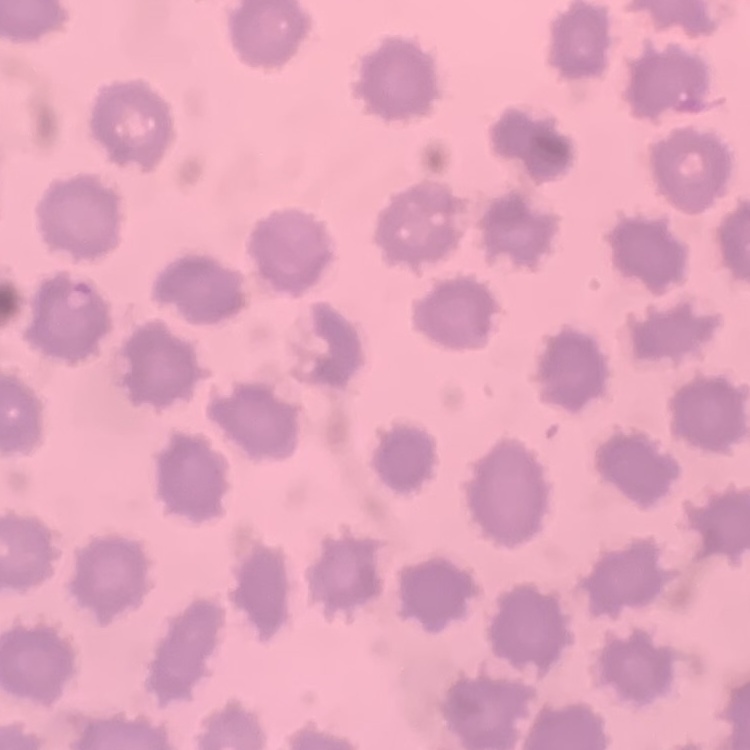

red blood cell morphology = no rouleaux formation
preparation = thin blood film
stain = Field's or Giemsa
image type = square crop of a larger photomicrograph